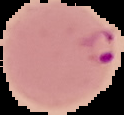
image type = cell region segmented out of the field of view; surrounding area masked to black
result = Plasmodium parasites detected
preparation = thin blood film
image size = 124×115 pixels